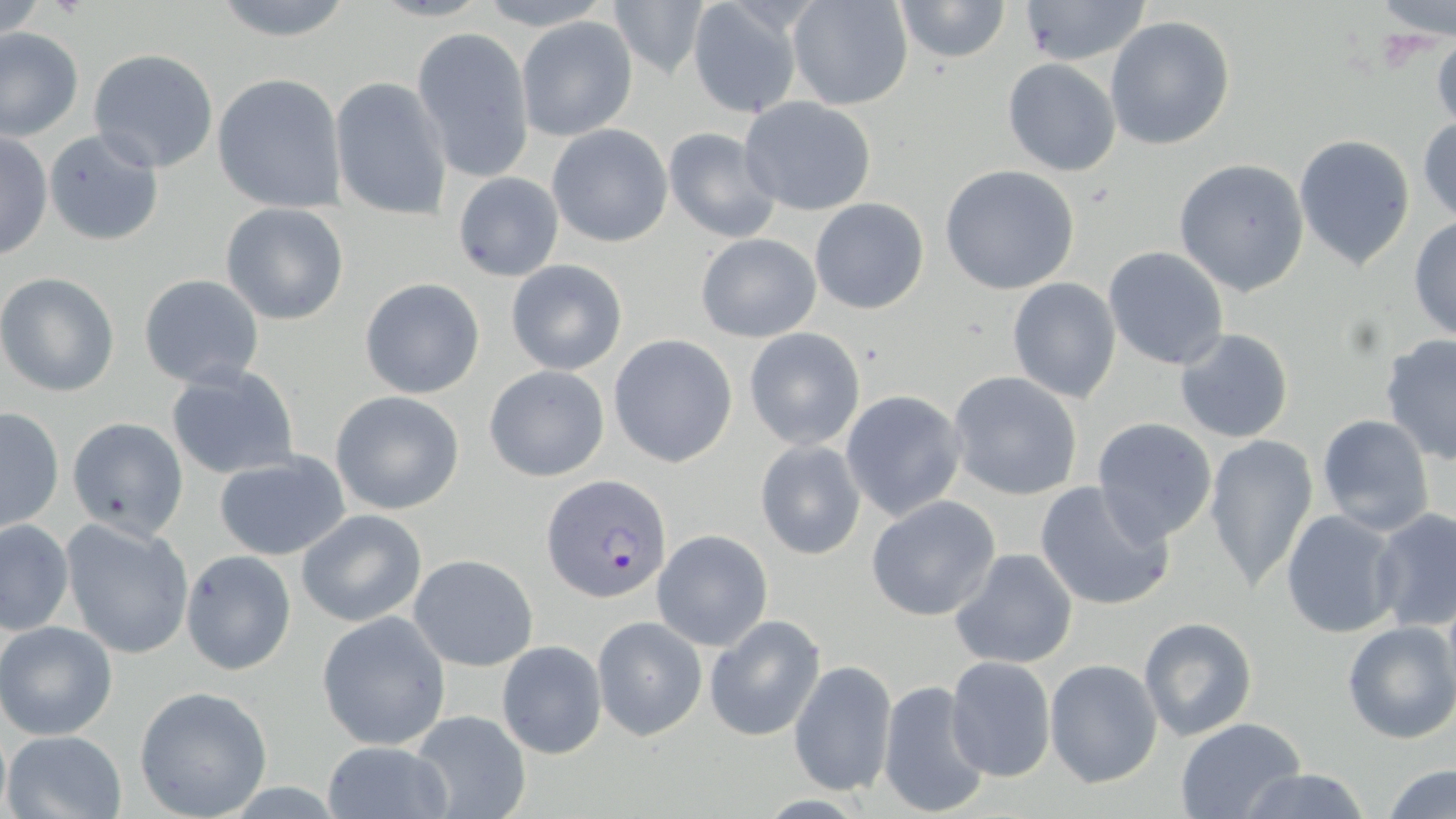 Approximate bounding boxes as named x1/y1/x2/y2 corners in pixels. Plasmodium falciparum-infected red blood cell locations: (x1=541, y1=473, x2=670, y2=605). Uninfected red blood cell locations: (x1=204, y1=0, x2=359, y2=43), (x1=474, y1=0, x2=611, y2=28), (x1=788, y1=0, x2=914, y2=111), (x1=892, y1=0, x2=1013, y2=65), (x1=1375, y1=0, x2=1455, y2=41), (x1=607, y1=1, x2=712, y2=79), (x1=1014, y1=2, x2=1150, y2=66), (x1=685, y1=3, x2=802, y2=119), (x1=516, y1=15, x2=638, y2=142), (x1=1103, y1=15, x2=1236, y2=152), (x1=412, y1=26, x2=536, y2=183), (x1=0, y1=27, x2=83, y2=140), (x1=1429, y1=32, x2=1456, y2=132), (x1=87, y1=48, x2=219, y2=172), (x1=1003, y1=58, x2=1122, y2=176), (x1=213, y1=73, x2=345, y2=213), (x1=330, y1=76, x2=453, y2=221), (x1=738, y1=96, x2=877, y2=216), (x1=1417, y1=115, x2=1456, y2=228), (x1=43, y1=125, x2=166, y2=248), (x1=546, y1=125, x2=673, y2=247), (x1=662, y1=126, x2=782, y2=243), (x1=0, y1=132, x2=51, y2=262), (x1=1293, y1=133, x2=1417, y2=270), (x1=1173, y1=158, x2=1309, y2=297), (x1=938, y1=165, x2=1081, y2=296), (x1=451, y1=172, x2=566, y2=281), (x1=809, y1=198, x2=929, y2=315), (x1=220, y1=202, x2=350, y2=325), (x1=1409, y1=215, x2=1456, y2=343), (x1=694, y1=232, x2=822, y2=342), (x1=1103, y1=246, x2=1229, y2=370), (x1=505, y1=259, x2=628, y2=376), (x1=0, y1=272, x2=120, y2=397), (x1=138, y1=274, x2=266, y2=389), (x1=359, y1=277, x2=486, y2=399), (x1=1007, y1=277, x2=1121, y2=404), (x1=1174, y1=327, x2=1295, y2=444), (x1=743, y1=328, x2=865, y2=451), (x1=608, y1=335, x2=739, y2=468), (x1=1379, y1=335, x2=1456, y2=465), (x1=164, y1=364, x2=300, y2=480), (x1=484, y1=364, x2=610, y2=482), (x1=947, y1=371, x2=1084, y2=501), (x1=330, y1=390, x2=466, y2=515), (x1=840, y1=390, x2=965, y2=521), (x1=1, y1=406, x2=65, y2=532), (x1=1316, y1=414, x2=1435, y2=535), (x1=1089, y1=416, x2=1219, y2=545), (x1=67, y1=417, x2=189, y2=540), (x1=1204, y1=434, x2=1318, y2=594), (x1=754, y1=439, x2=866, y2=560), (x1=212, y1=451, x2=352, y2=561), (x1=1033, y1=481, x2=1174, y2=612), (x1=866, y1=495, x2=1001, y2=621), (x1=1370, y1=508, x2=1456, y2=632), (x1=296, y1=509, x2=427, y2=626), (x1=1281, y1=509, x2=1402, y2=641), (x1=61, y1=517, x2=195, y2=660), (x1=0, y1=520, x2=74, y2=635), (x1=652, y1=530, x2=774, y2=651), (x1=948, y1=548, x2=1079, y2=672), (x1=181, y1=550, x2=296, y2=676), (x1=409, y1=554, x2=538, y2=671), (x1=317, y1=612, x2=451, y2=751), (x1=704, y1=615, x2=826, y2=742), (x1=1136, y1=615, x2=1257, y2=742), (x1=592, y1=616, x2=706, y2=741), (x1=0, y1=620, x2=118, y2=741), (x1=1343, y1=621, x2=1456, y2=744), (x1=496, y1=640, x2=607, y2=758), (x1=945, y1=656, x2=1056, y2=783), (x1=789, y1=659, x2=898, y2=800), (x1=1044, y1=659, x2=1161, y2=788), (x1=876, y1=679, x2=991, y2=819), (x1=134, y1=686, x2=273, y2=819), (x1=405, y1=709, x2=532, y2=819), (x1=1174, y1=717, x2=1306, y2=819), (x1=3, y1=730, x2=127, y2=819), (x1=320, y1=740, x2=452, y2=819), (x1=1383, y1=764, x2=1456, y2=819), (x1=1232, y1=768, x2=1373, y2=819). Slide-level diagnosis: Plasmodium falciparum. One field of a larger specimen. Thin blood smear. Image is 1456×819 pixels. May-Grünwald-Giemsa stain. Optical microscopy. 1000x magnification.